Comment on the morphology of the erythrocytes.
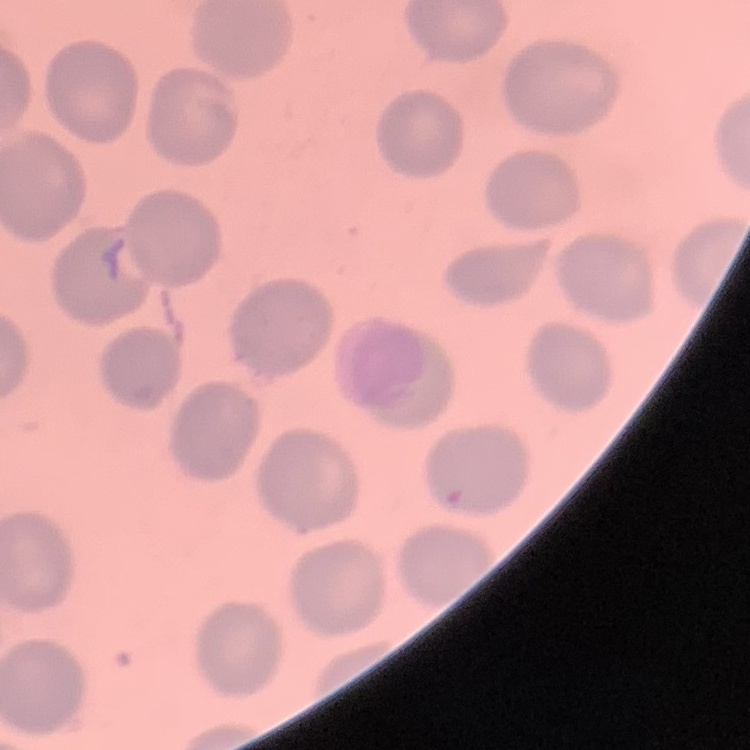
They show no rouleaux formation.

Summary:
  - Stain: Field's or Giemsa
  - Preparation: thin blood smear
  - Image type: square crop of a larger photomicrograph